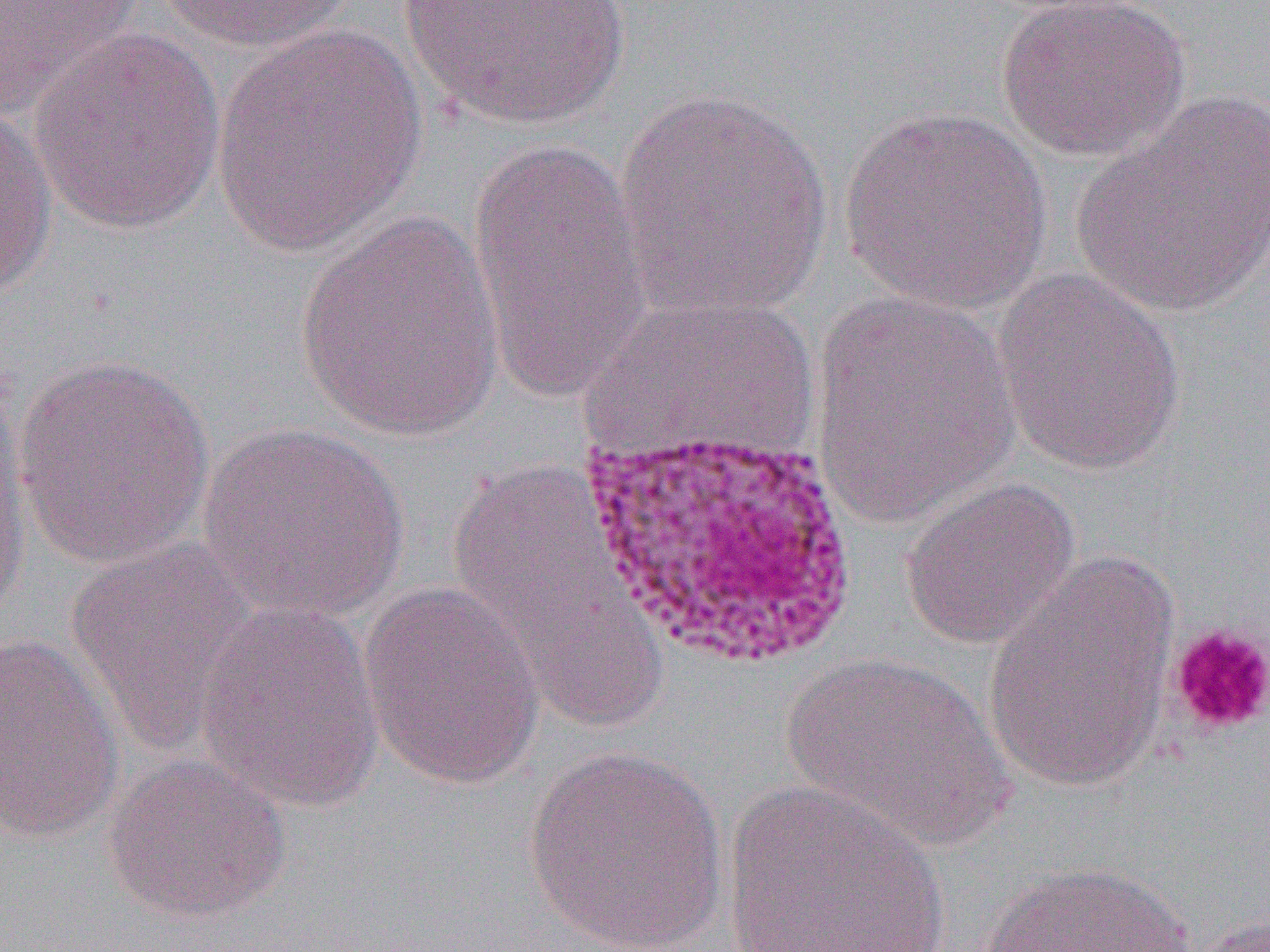

Summary:
  - Coordinate format: approximate bounding boxes as [x1, y1, x2, y2] in pixels
  - Uninfected red blood cell locations: [0, 0, 146, 122], [158, 0, 360, 52], [994, 0, 1191, 163], [398, 1, 633, 132], [211, 23, 429, 258], [28, 28, 228, 236], [615, 89, 834, 323], [1073, 94, 1270, 318], [0, 101, 58, 303], [838, 106, 1053, 315], [465, 135, 653, 402], [294, 211, 506, 443], [991, 268, 1188, 476], [808, 290, 1022, 529], [12, 354, 215, 569], [196, 422, 409, 621], [0, 441, 30, 640], [444, 458, 666, 731], [899, 477, 1081, 650], [65, 535, 265, 756], [982, 549, 1183, 794], [356, 580, 546, 790], [194, 601, 386, 812], [0, 631, 125, 845], [783, 652, 1013, 849], [523, 745, 729, 950], [102, 754, 292, 924], [723, 779, 951, 952], [978, 861, 1198, 952], [1185, 913, 1270, 952]
  - Platelet locations: [1167, 622, 1270, 737]
  - Slide-level diagnosis: Plasmodium vivax
  - Modality: optical microscopy
  - Magnification: 1000x
  - Preparation: thin blood film
  - Image size: 1270×952 pixels
  - Field of view: one of a larger specimen